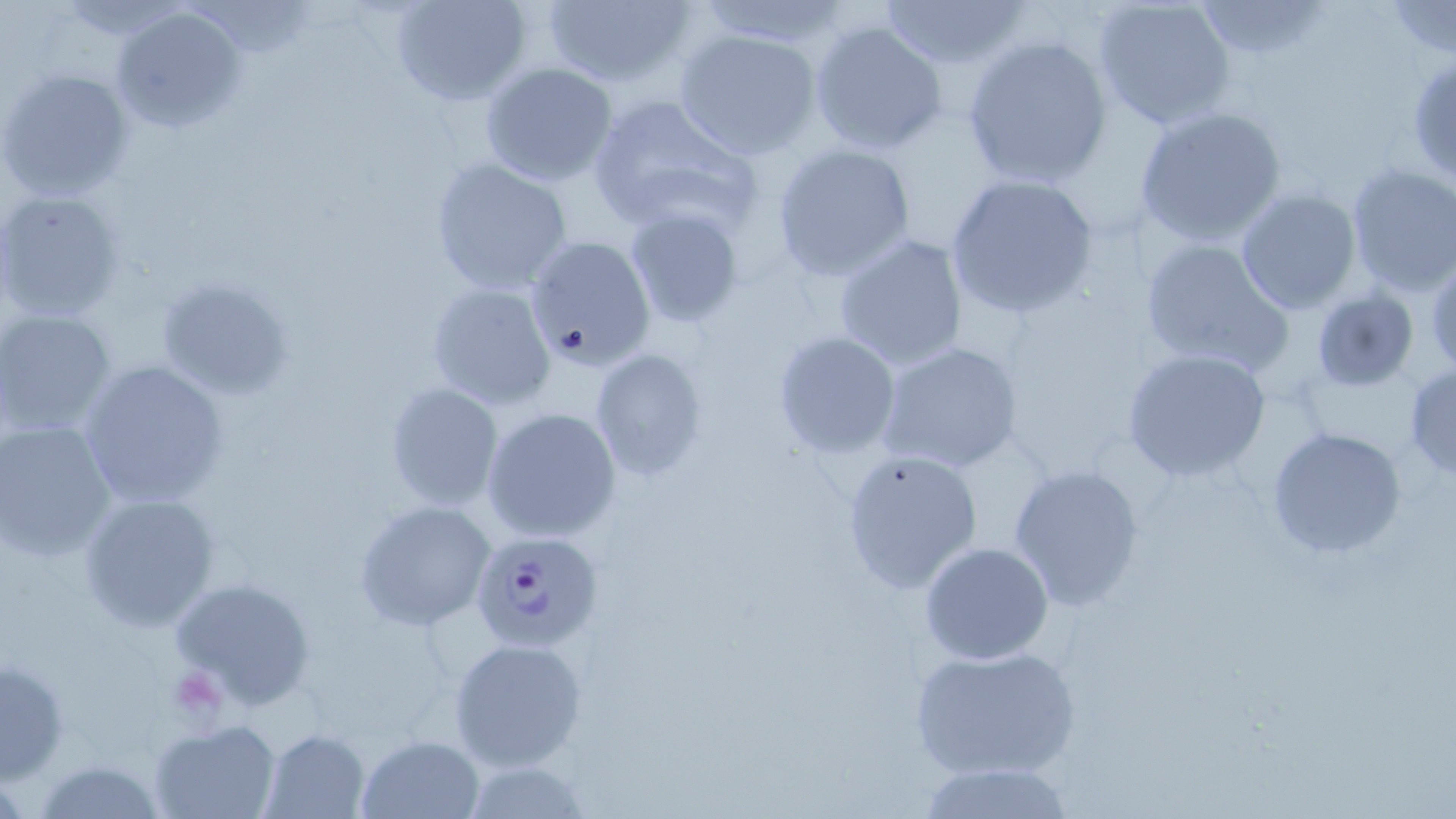
{
  "slide_level_diagnosis": "Plasmodium falciparum",
  "preparation": "thin blood film",
  "field_of_view": "one of a larger specimen",
  "plasmodium_falciparum_infected_red_blood_cell_locations": "approximate bounding boxes as named x1/y1/x2/y2 corners in pixels: (x1=472, y1=529, x2=603, y2=648)",
  "platelet_locations": "approximate bounding boxes as named x1/y1/x2/y2 corners in pixels: (x1=176, y1=667, x2=232, y2=717)",
  "uninfected_red_blood_cell_locations": "approximate bounding boxes as named x1/y1/x2/y2 corners in pixels: (x1=388, y1=0, x2=534, y2=108), (x1=537, y1=0, x2=698, y2=89), (x1=879, y1=0, x2=1028, y2=71), (x1=1091, y1=0, x2=1237, y2=131), (x1=692, y1=1, x2=854, y2=53), (x1=1192, y1=1, x2=1331, y2=59), (x1=1384, y1=1, x2=1456, y2=57), (x1=109, y1=6, x2=248, y2=134), (x1=807, y1=17, x2=950, y2=156), (x1=675, y1=29, x2=823, y2=158), (x1=959, y1=35, x2=1114, y2=189), (x1=1406, y1=56, x2=1456, y2=188), (x1=479, y1=61, x2=619, y2=187), (x1=0, y1=67, x2=133, y2=200), (x1=584, y1=93, x2=761, y2=235), (x1=1135, y1=105, x2=1288, y2=245), (x1=771, y1=142, x2=917, y2=280), (x1=428, y1=156, x2=575, y2=297), (x1=1345, y1=163, x2=1456, y2=295), (x1=943, y1=173, x2=1100, y2=318), (x1=1235, y1=189, x2=1362, y2=312), (x1=1, y1=191, x2=124, y2=321), (x1=624, y1=207, x2=746, y2=329), (x1=830, y1=232, x2=970, y2=372), (x1=523, y1=235, x2=657, y2=371), (x1=1138, y1=237, x2=1293, y2=376), (x1=1426, y1=252, x2=1456, y2=377), (x1=153, y1=274, x2=298, y2=403), (x1=426, y1=281, x2=557, y2=411), (x1=1313, y1=289, x2=1420, y2=392), (x1=0, y1=308, x2=118, y2=437), (x1=771, y1=330, x2=901, y2=460), (x1=874, y1=340, x2=1025, y2=475), (x1=1120, y1=348, x2=1271, y2=483), (x1=589, y1=349, x2=708, y2=482), (x1=77, y1=359, x2=229, y2=508), (x1=1405, y1=363, x2=1456, y2=479), (x1=384, y1=383, x2=503, y2=511), (x1=481, y1=406, x2=624, y2=543), (x1=0, y1=419, x2=118, y2=559), (x1=1266, y1=426, x2=1407, y2=560), (x1=840, y1=447, x2=982, y2=593), (x1=1008, y1=462, x2=1145, y2=611), (x1=76, y1=491, x2=223, y2=631), (x1=354, y1=499, x2=494, y2=632), (x1=918, y1=542, x2=1056, y2=665), (x1=167, y1=575, x2=317, y2=709), (x1=447, y1=636, x2=589, y2=773), (x1=908, y1=642, x2=1082, y2=781), (x1=1, y1=656, x2=70, y2=783), (x1=150, y1=719, x2=280, y2=819), (x1=259, y1=728, x2=369, y2=817), (x1=356, y1=734, x2=483, y2=817), (x1=31, y1=759, x2=171, y2=818), (x1=460, y1=759, x2=589, y2=816), (x1=914, y1=760, x2=1075, y2=819)",
  "magnification": "1000x",
  "modality": "optical microscopy",
  "stain": "May-Grünwald-Giemsa",
  "image_size": "1456×819 pixels"
}